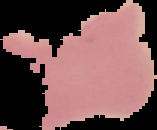
Summary:
  - Result: malaria parasites detected
  - Preparation: thin blood smear
  - Image size: 157×130 pixels
  - Image type: cell region segmented out of the field of view; surrounding area masked to black